Outline each uninfected red blood cell.
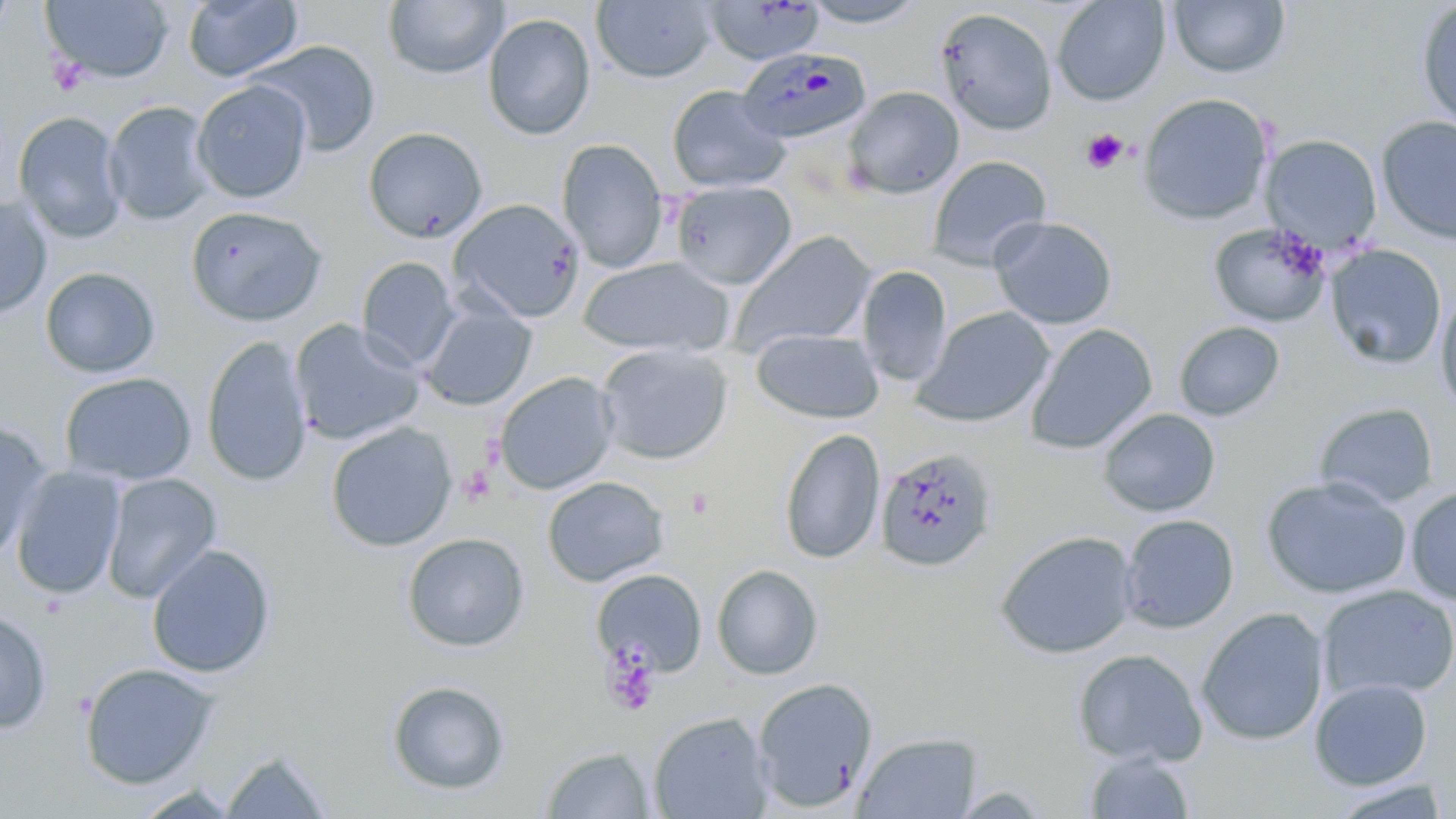
Approximate bounding boxes as (x1,y1)-(x2,y2) corner pairs in pixels.
Uninfected red blood cells: (40,0)-(173,84), (382,0)-(509,79), (801,0)-(930,28), (1052,0)-(1170,106), (182,1)-(304,83), (592,1)-(717,83), (704,1)-(826,66), (1167,1)-(1290,78), (1415,2)-(1456,132), (935,7)-(1057,135), (482,12)-(596,141), (251,40)-(381,158), (192,80)-(312,203), (666,84)-(791,194), (843,86)-(964,200), (1137,92)-(1274,225), (103,100)-(216,226), (13,111)-(128,243), (1375,115)-(1456,246), (363,127)-(488,243), (1261,134)-(1382,251), (556,138)-(669,272), (926,155)-(1052,270), (671,180)-(797,289), (0,195)-(53,319), (449,198)-(586,323), (185,205)-(328,326), (989,216)-(1118,329), (1209,222)-(1331,328), (729,231)-(879,355), (1324,245)-(1446,369), (578,256)-(736,358), (357,257)-(459,371), (856,265)-(952,387), (40,267)-(160,378), (1434,288)-(1456,415), (419,300)-(536,411), (913,306)-(1056,428), (290,319)-(426,446), (1173,321)-(1285,421), (1024,323)-(1158,454), (750,328)-(884,423), (201,335)-(313,487), (595,342)-(733,465), (494,371)-(619,495), (59,372)-(197,486), (1313,401)-(1440,509), (1098,408)-(1221,517), (0,419)-(52,561), (325,423)-(458,552), (778,428)-(886,565), (875,447)-(997,573), (10,465)-(126,600), (101,473)-(221,603), (541,476)-(668,587), (1260,476)-(1412,599), (1406,485)-(1456,606), (1120,514)-(1240,633), (995,530)-(1139,659), (402,532)-(529,652), (146,543)-(276,679), (711,564)-(823,680), (591,568)-(708,678), (1318,584)-(1456,701), (0,607)-(52,734), (1196,607)-(1329,746), (1073,648)-(1206,767), (78,661)-(219,790), (752,677)-(878,812), (1309,679)-(1433,790), (387,680)-(510,796), (648,711)-(774,819), (852,732)-(982,818), (541,746)-(656,818), (221,749)-(333,818), (1084,750)-(1196,818), (1327,779)-(1453,819).

Platelet locations: (1081,128)-(1129,174), (685,488)-(713,519), (601,643)-(661,718). Plasmodium malariae-infected red blood cell locations: (737,46)-(873,145). Slide-level diagnosis: Plasmodium malariae. May-Grünwald-Giemsa stain. One field of a larger specimen. Thin blood film. Optical microscopy. Captured at 1000x magnification. Image is 1456×819 pixels.